Evaluate for malaria.
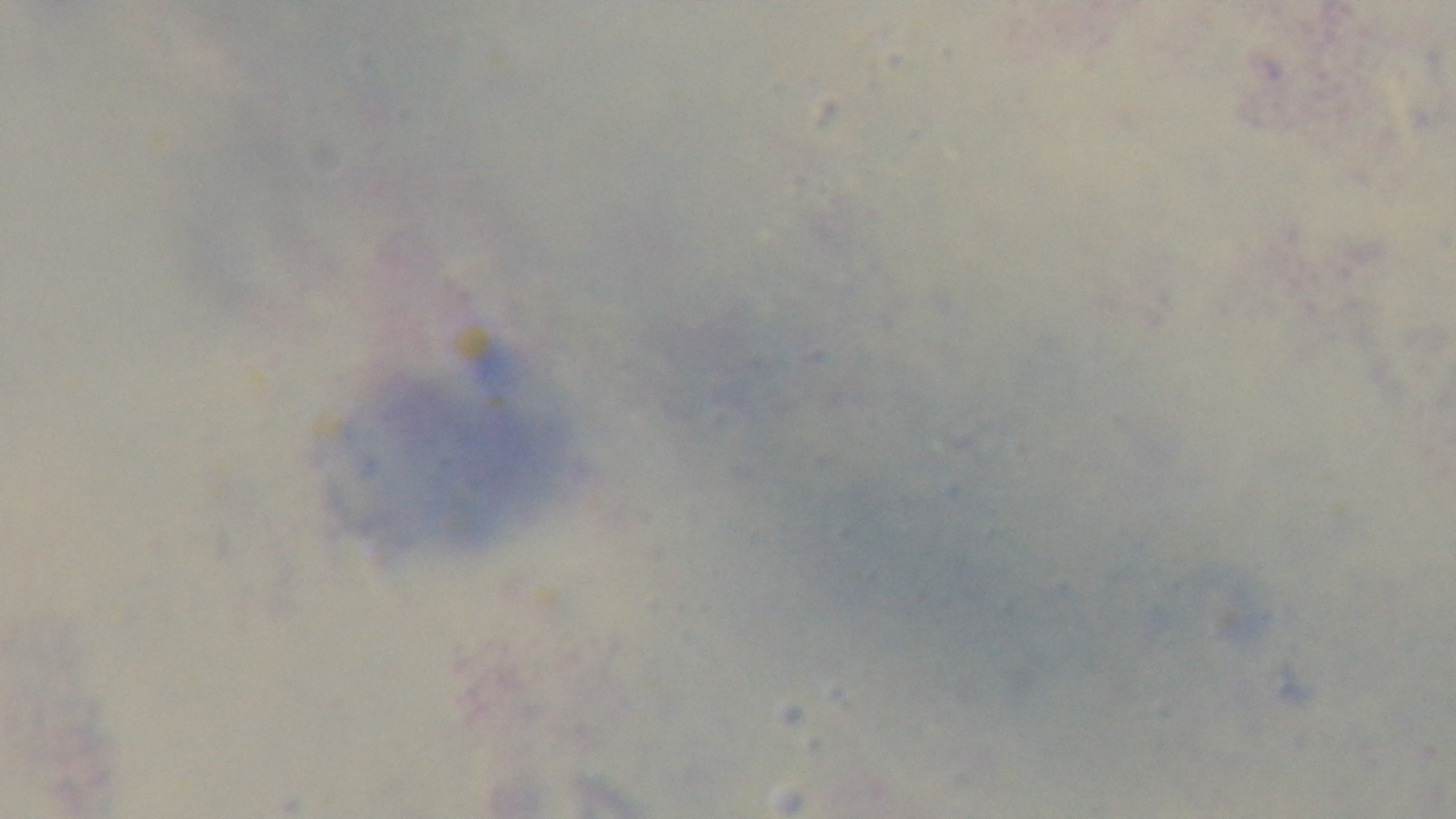

Uninfected.

Captured with a mounted 4K digital camera. Oil-immersion objective, 100x. Preparation: thick blood film. Single field of view. Photomicrograph. Giemsa-stained.